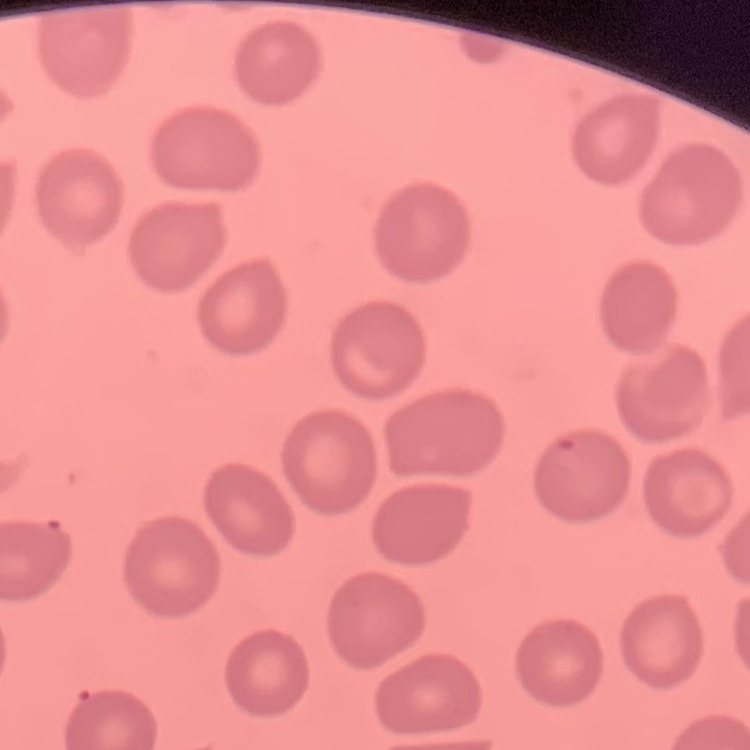
{
  "erythrocyte_morphology": "no rouleaux formation",
  "image_type": "one tile cut from a larger photomicrograph",
  "preparation": "thin blood film",
  "stain": "Field's or Giemsa"
}